Classify this cell by malaria status.
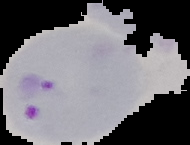
It is parasitized.

preparation = thin blood smear
image size = 190×145 pixels
image type = cell region segmented out of the field of view; surrounding area masked to black